Name the blood parasite species.
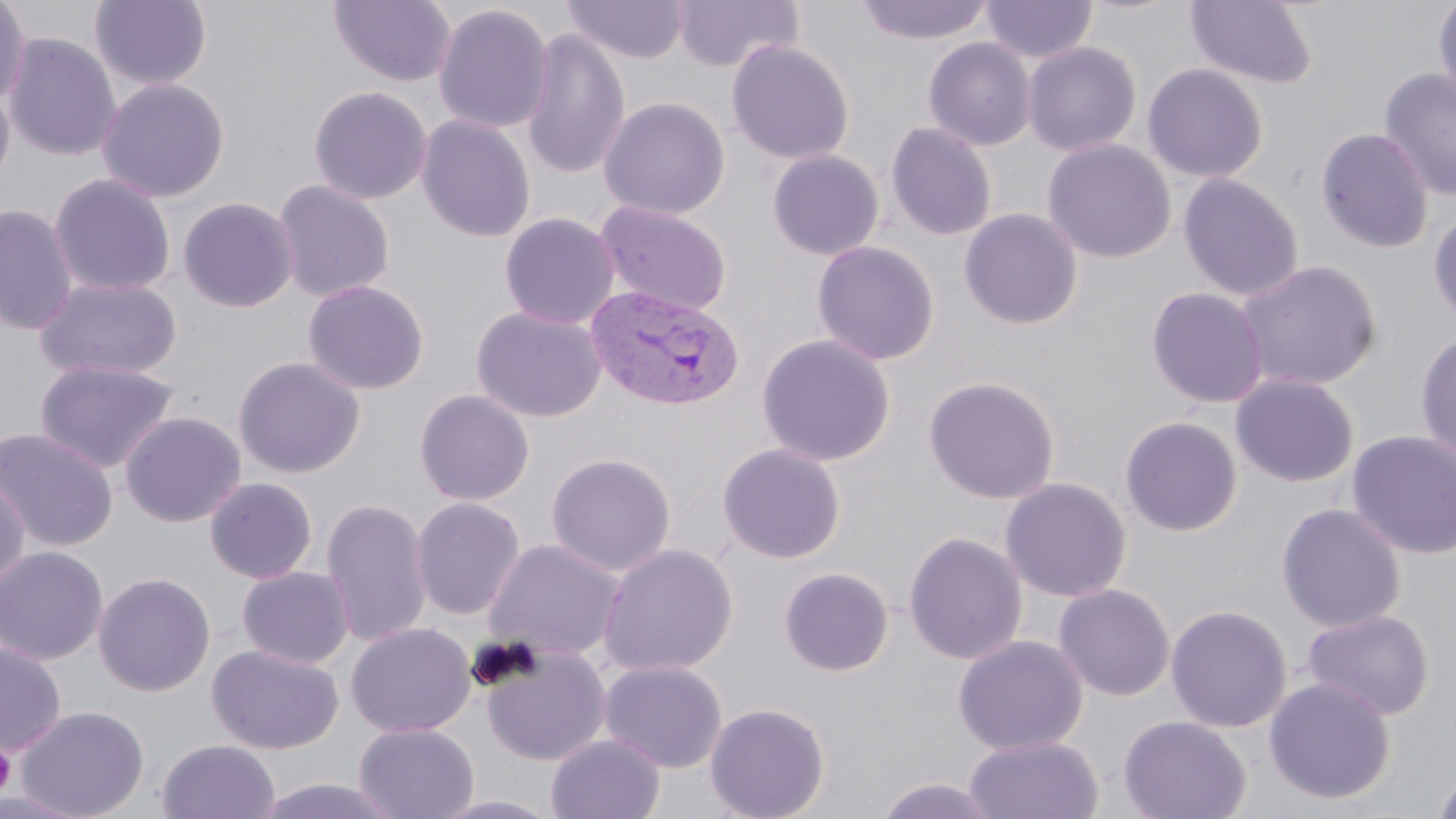

Plasmodium vivax.

Summary:
  - Coordinate format: approximate bounding boxes as [x1, y1, x2, y2] in pixels
  - Plasmodium vivax-infected red blood cell locations: [585, 284, 743, 411]
  - Platelet locations: [0, 741, 16, 801]
  - Uninfected red blood cell locations: [90, 0, 212, 90], [328, 0, 456, 87], [562, 0, 690, 63], [672, 0, 802, 73], [855, 0, 995, 45], [982, 0, 1097, 64], [1185, 0, 1319, 90], [1433, 0, 1456, 109], [0, 1, 31, 106], [433, 4, 554, 134], [521, 26, 631, 180], [3, 32, 121, 161], [923, 37, 1035, 151], [726, 39, 855, 165], [1023, 41, 1142, 156], [1142, 63, 1268, 183], [1378, 68, 1456, 202], [96, 77, 230, 202], [0, 80, 15, 191], [308, 86, 432, 205], [598, 96, 730, 220], [416, 114, 536, 243], [886, 122, 997, 241], [1316, 127, 1434, 254], [1042, 138, 1177, 264], [767, 149, 884, 261], [48, 173, 176, 297], [1177, 173, 1303, 301], [272, 180, 395, 302], [178, 196, 299, 313], [595, 201, 732, 317], [0, 204, 79, 335], [1428, 205, 1456, 329], [959, 208, 1083, 329], [499, 212, 620, 329], [811, 240, 940, 366], [1234, 259, 1382, 392], [33, 277, 183, 382], [303, 279, 429, 395], [1146, 286, 1269, 409], [472, 306, 608, 423], [1415, 328, 1456, 465], [756, 333, 896, 467], [233, 356, 365, 479], [34, 359, 180, 474], [1230, 373, 1359, 488], [923, 375, 1060, 504], [414, 388, 535, 506], [120, 410, 246, 528], [1119, 416, 1242, 537], [0, 427, 118, 552], [1346, 430, 1456, 561], [717, 442, 846, 563], [546, 452, 676, 576], [0, 471, 30, 592], [205, 477, 318, 583], [1000, 477, 1132, 602], [411, 497, 525, 620], [320, 498, 432, 647], [1275, 502, 1407, 632], [904, 531, 1027, 664], [482, 538, 626, 661], [598, 542, 738, 676], [0, 545, 108, 665], [237, 566, 354, 668], [779, 567, 894, 676], [94, 572, 215, 696], [1053, 583, 1176, 701], [1166, 604, 1293, 732], [1302, 608, 1434, 722], [346, 622, 476, 737], [952, 634, 1088, 755], [0, 642, 66, 755], [479, 643, 611, 766], [207, 644, 343, 754], [599, 660, 727, 773], [1263, 676, 1396, 804], [704, 702, 830, 819], [16, 704, 150, 819], [1118, 715, 1251, 819], [353, 723, 479, 819], [546, 733, 665, 819], [964, 735, 1104, 819], [157, 739, 281, 819], [1431, 763, 1456, 819], [874, 776, 1002, 818], [253, 777, 405, 819], [0, 790, 89, 818], [430, 793, 566, 818]
  - Modality: optical microscopy
  - Field of view: single
  - Magnification: 1000x
  - Preparation: thin blood smear
  - Image size: 1456×819 pixels
  - Stain: May-Grünwald-Giemsa